Identify the parasite.
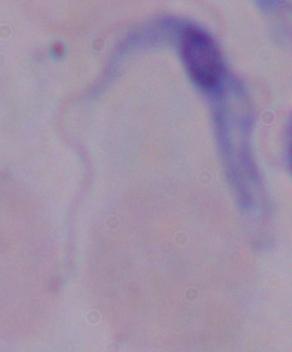

A trypanosome.

{
  "modality": "photomicrograph",
  "magnification": "1000x"
}